Assess the morphology of the erythrocytes.
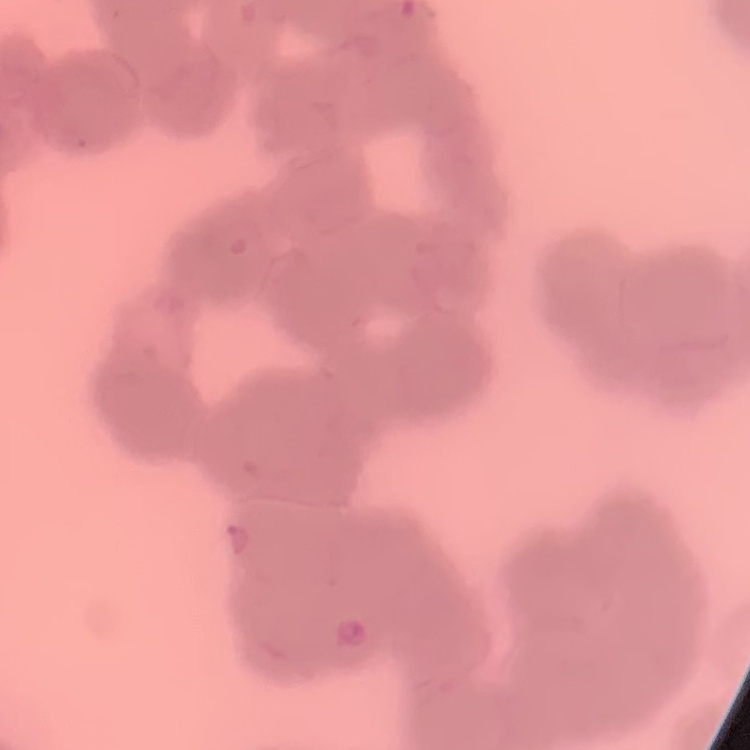

Rouleaux formation.

Stained with either Field's or Giemsa. Thin blood film. Square crop of a larger photomicrograph.